Locate every blood parasite and identify its species.
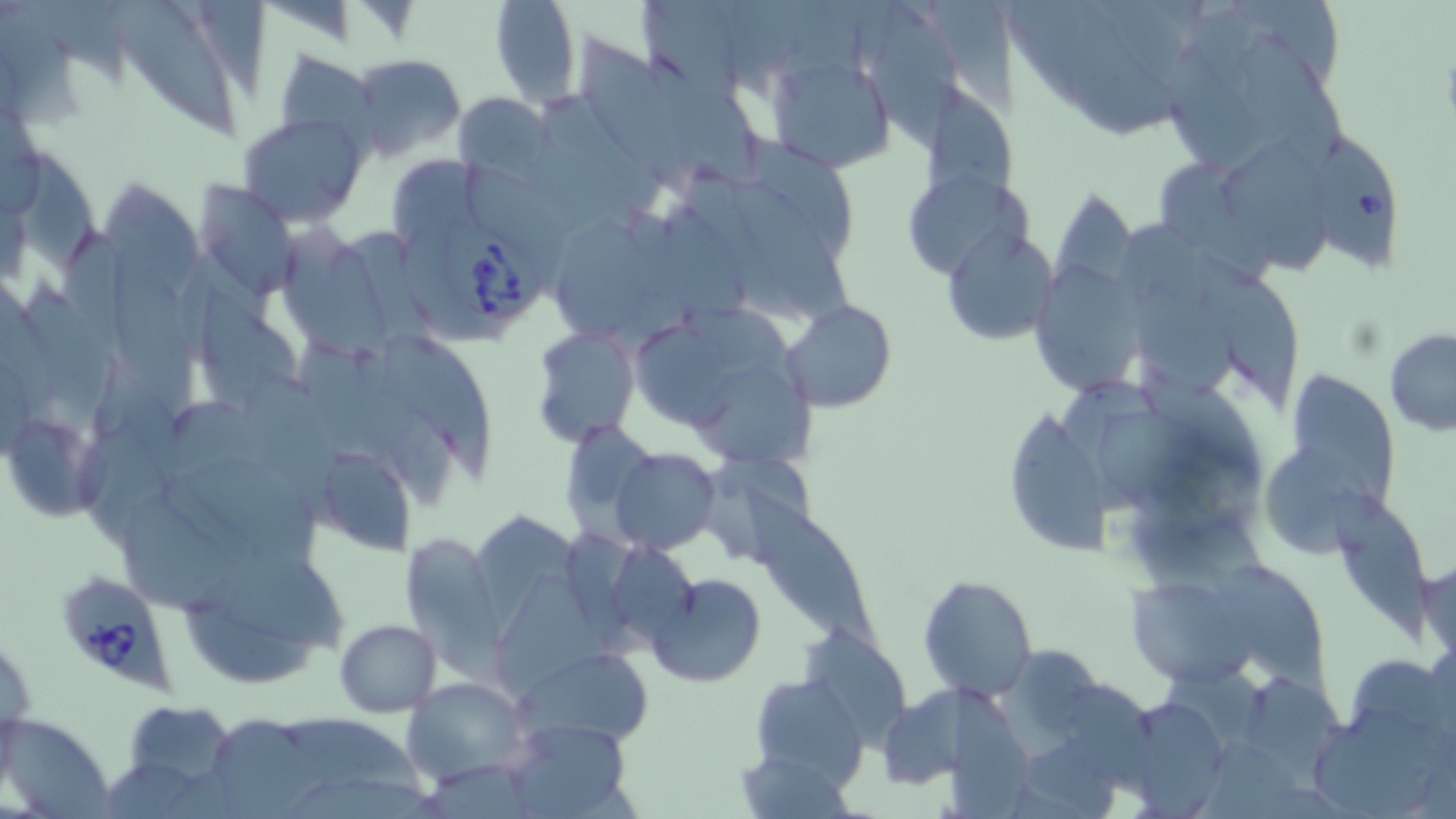
Approximate bounding boxes as (x1, y1, x2, y2) in pixels.
Babesia divergens-infected red blood cells: (1301, 136, 1406, 270), (440, 217, 551, 327), (54, 569, 180, 696).
No Plasmodium falciparum, Plasmodium ovale, Plasmodium malariae, Plasmodium vivax, or Trypanosoma brucei observed.

Summary:
  - Uninfected red blood cell locations: (490, 0, 580, 108), (868, 3, 967, 159), (1058, 8, 1190, 139), (1232, 22, 1344, 173), (576, 28, 702, 205), (123, 42, 242, 150), (766, 47, 898, 176), (273, 49, 377, 143), (349, 53, 468, 162), (647, 53, 762, 194), (924, 84, 1032, 237), (452, 91, 552, 185), (541, 91, 672, 219), (238, 113, 367, 228), (1218, 135, 1335, 282), (1166, 165, 1274, 284), (98, 174, 213, 345), (908, 177, 1046, 285), (194, 181, 297, 296), (730, 181, 860, 337), (274, 219, 398, 358), (559, 221, 664, 345), (943, 226, 1060, 349), (1190, 243, 1307, 417), (105, 248, 208, 435), (1035, 259, 1151, 408), (1135, 282, 1247, 412), (782, 301, 896, 413), (637, 315, 744, 433), (531, 327, 639, 446), (385, 329, 502, 482), (1384, 329, 1456, 435), (241, 365, 346, 507), (688, 366, 822, 467), (1281, 368, 1402, 516), (1003, 414, 1123, 564), (8, 415, 117, 523), (569, 425, 672, 546), (1259, 441, 1390, 562), (309, 443, 419, 556), (610, 448, 720, 552), (743, 486, 886, 664), (1329, 487, 1432, 643), (119, 495, 246, 620), (396, 536, 502, 663), (223, 543, 354, 660), (1419, 553, 1455, 667), (1215, 558, 1335, 702), (488, 565, 633, 711), (646, 570, 767, 687), (920, 572, 1037, 702), (183, 574, 319, 688), (1121, 576, 1256, 688), (334, 619, 442, 718), (804, 625, 919, 752), (990, 640, 1108, 779), (517, 644, 657, 748), (748, 673, 867, 787), (401, 676, 529, 785), (1245, 676, 1355, 791), (1062, 677, 1166, 797), (876, 688, 972, 790), (117, 699, 239, 796), (1133, 699, 1228, 819), (1313, 702, 1440, 819), (213, 711, 325, 819), (4, 713, 113, 818), (283, 716, 437, 800), (503, 718, 633, 818)
  - Slide-level diagnosis: Babesia divergens
  - Image size: 1456×819 pixels
  - Modality: optical microscopy
  - Stain: May-Grünwald-Giemsa
  - Preparation: thin blood film
  - Field of view: one of a larger specimen
  - Magnification: 1000x